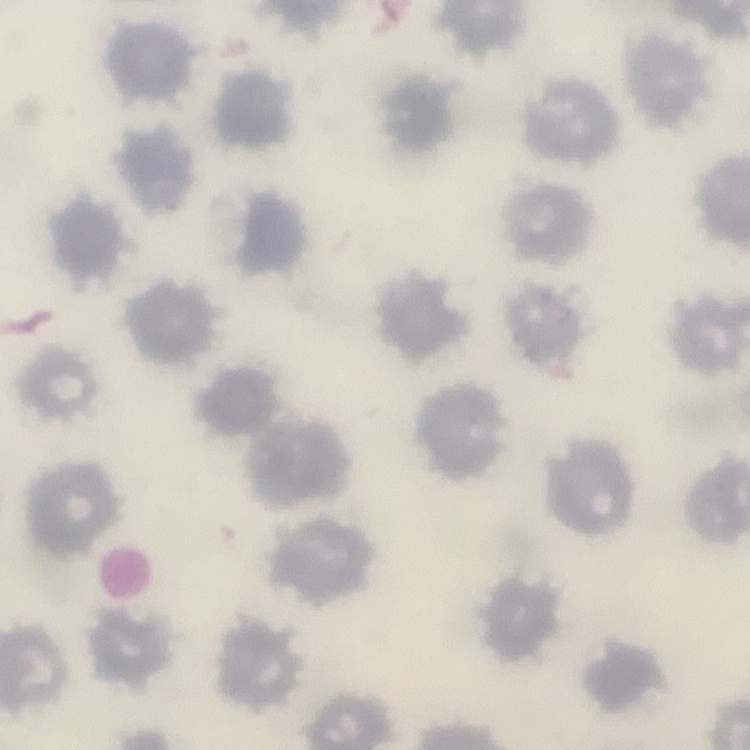 The erythrocytes exhibit no rouleaux formation. One tile cut from a larger photomicrograph. Stained with either Field's or Giemsa. Thin blood smear.